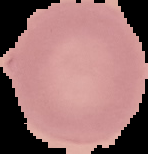
{
  "malaria_status": "uninfected",
  "preparation": "thin blood film",
  "image_size": "148×154 pixels",
  "image_type": "cell region segmented out of the field of view; surrounding area masked to black"
}